Assess this cell for malaria.
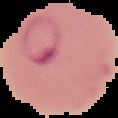

Parasitized.

Summary:
  - Preparation: thin blood film
  - Image size: 118×118 pixels
  - Image type: segmented cell region with the area outside set to black